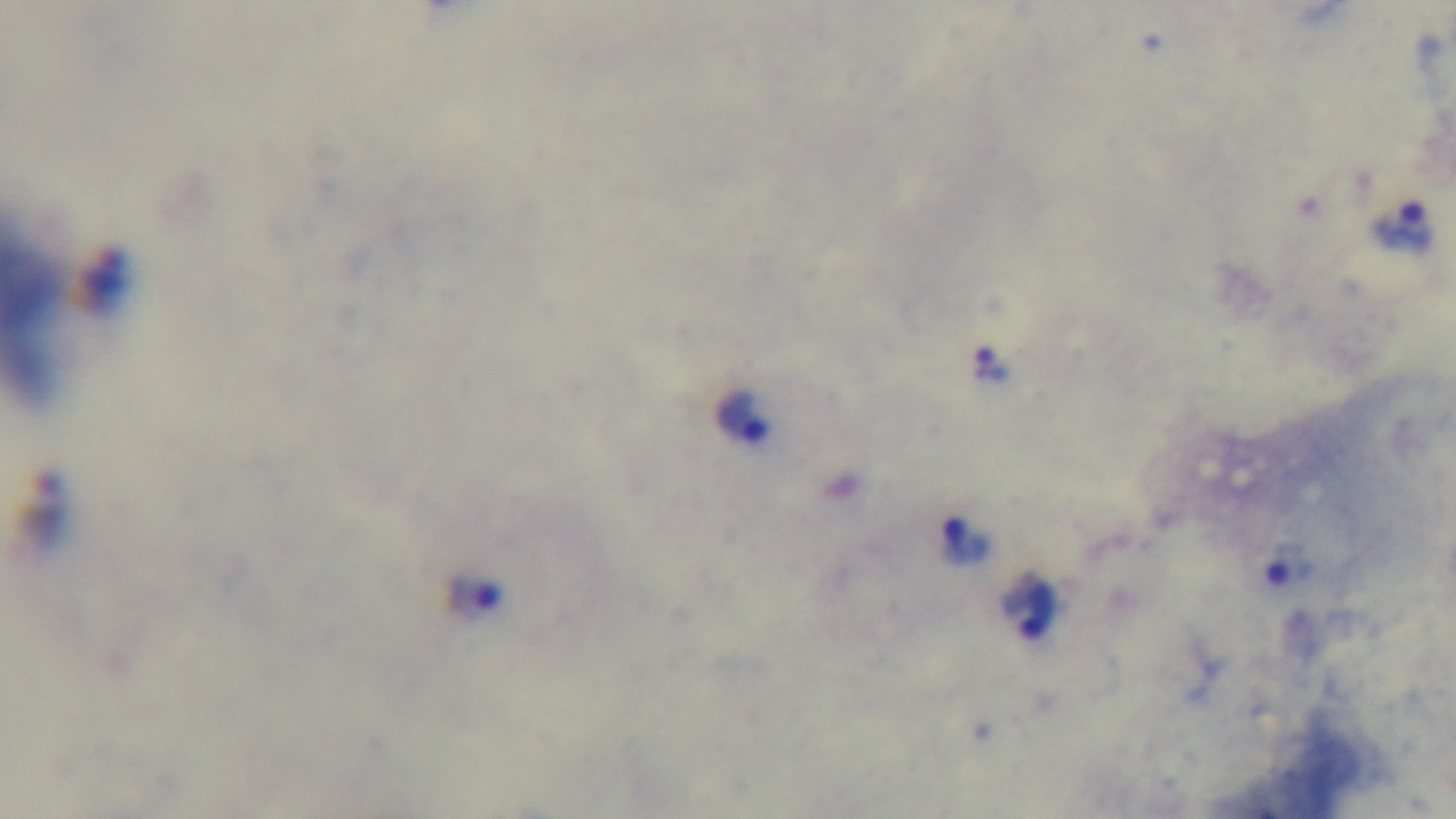
Malaria status: positive. Mounted 4K digital camera. One field from the slide. Oil-immersion objective, 100x. Preparation: thick. Light microscopy. Giemsa stain.